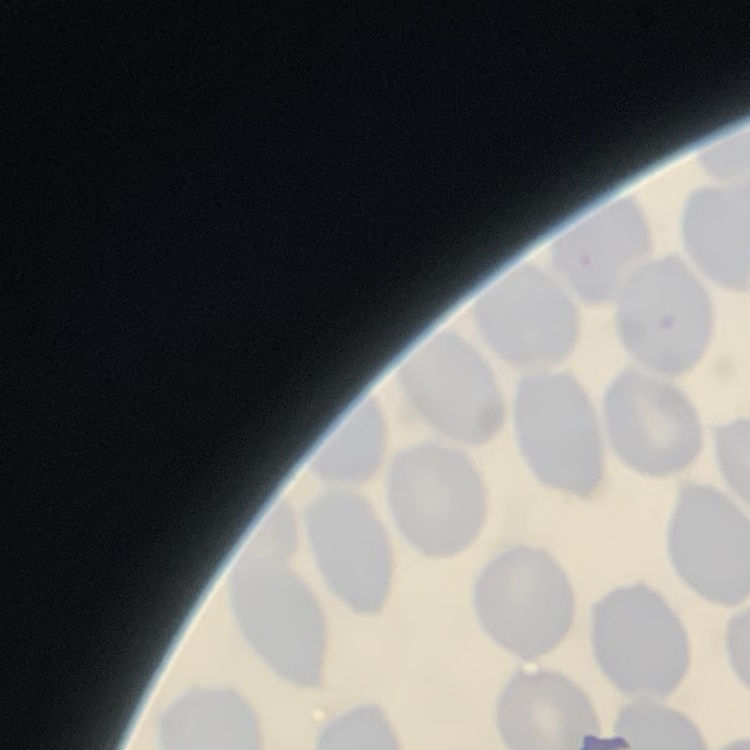 The erythrocytes show no rouleaux formation. One tile cut from a larger photomicrograph. Stained with either Field's or Giemsa. Thin blood film.